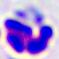 Captured at 400x magnification. A white blood cell is shown. Photomicrograph.